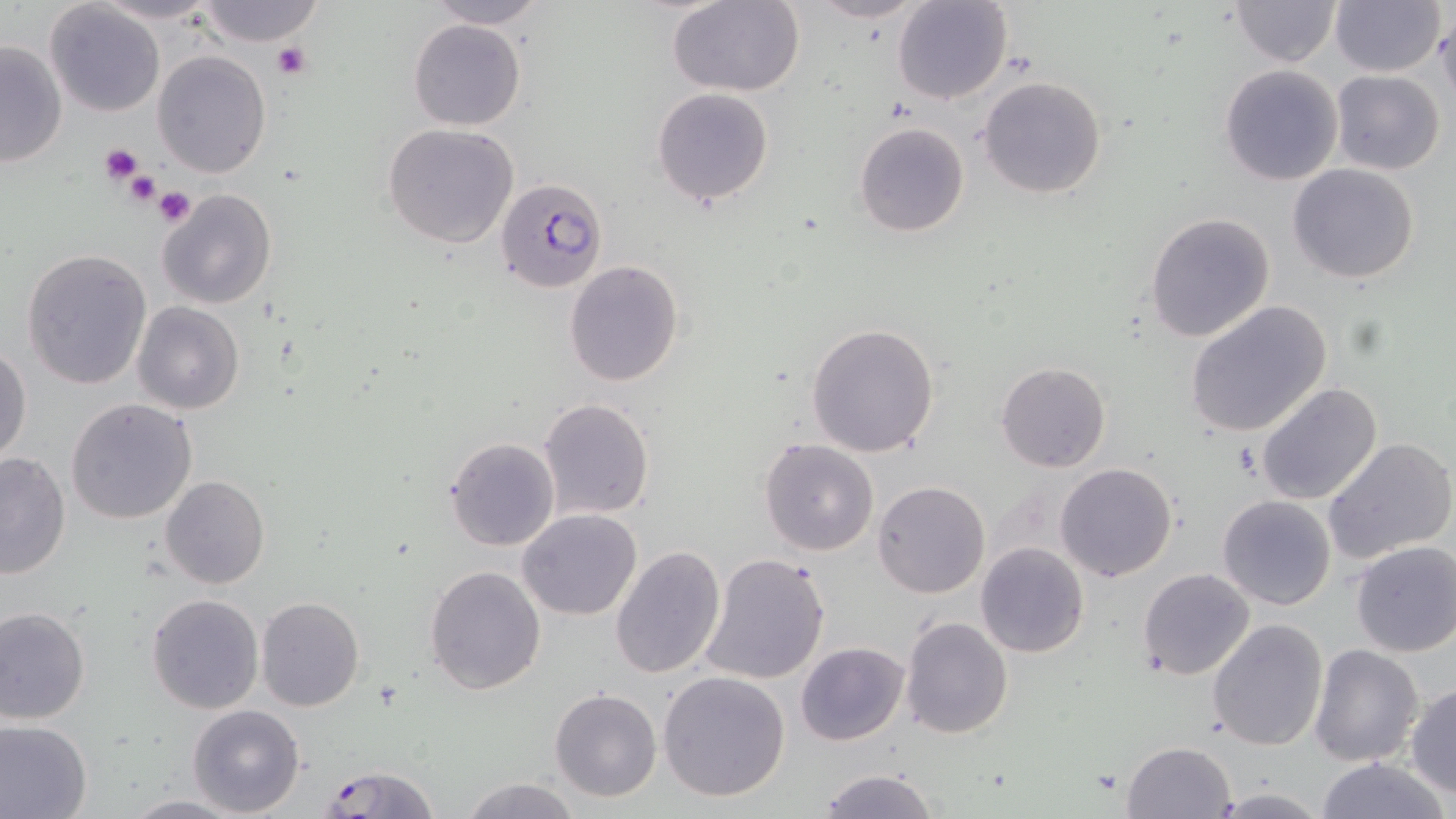
Summary:
  - Coordinate format: approximate bounding boxes as [x1, y1, x2, y2] in pixels
  - Plasmodium falciparum-infected red blood cell locations: [496, 176, 606, 296]
  - Platelet locations: [271, 41, 310, 79], [99, 143, 144, 185], [119, 170, 164, 211], [154, 186, 197, 228]
  - Uninfected red blood cell locations: [94, 0, 225, 25], [198, 0, 328, 47], [423, 0, 549, 28], [805, 0, 929, 25], [893, 0, 1014, 104], [1229, 0, 1340, 67], [666, 1, 804, 96], [1329, 1, 1445, 76], [44, 2, 166, 117], [1436, 15, 1456, 105], [408, 19, 526, 131], [0, 40, 69, 167], [153, 49, 271, 178], [1219, 64, 1343, 185], [1331, 69, 1445, 174], [978, 75, 1107, 200], [652, 87, 775, 207], [855, 121, 969, 238], [382, 123, 520, 249], [1287, 163, 1421, 283], [156, 188, 277, 309], [1145, 212, 1275, 341], [22, 249, 152, 391], [563, 260, 685, 387], [1185, 299, 1333, 438], [133, 303, 243, 415], [805, 322, 941, 458], [0, 342, 32, 463], [996, 361, 1110, 473], [1256, 381, 1384, 504], [65, 398, 198, 525], [535, 398, 655, 521], [445, 436, 560, 551], [759, 437, 879, 557], [1325, 437, 1456, 562], [0, 451, 71, 578], [1054, 463, 1178, 583], [160, 476, 269, 589], [873, 480, 990, 599], [1216, 494, 1337, 611], [517, 509, 642, 620], [1350, 540, 1456, 656], [975, 542, 1089, 657], [609, 545, 725, 682], [699, 552, 830, 687], [424, 565, 547, 695], [1136, 567, 1255, 681], [146, 593, 264, 714], [255, 598, 366, 712], [0, 608, 90, 726], [900, 616, 1013, 738], [1208, 620, 1328, 752], [795, 641, 909, 746], [1309, 643, 1425, 766], [658, 670, 790, 802], [1405, 683, 1456, 798], [549, 688, 662, 802], [188, 705, 306, 816], [0, 719, 93, 819], [1120, 740, 1237, 819], [1314, 757, 1449, 819], [317, 764, 440, 818], [817, 768, 940, 818], [459, 777, 580, 818], [1208, 787, 1330, 818], [122, 793, 242, 818]
  - Slide-level diagnosis: Plasmodium falciparum
  - Modality: light microscopy
  - Stain: May-Grünwald-Giemsa
  - Field of view: one of a larger specimen
  - Magnification: 1000x
  - Image size: 1456×819 pixels
  - Preparation: thin blood film